Locate platelets.
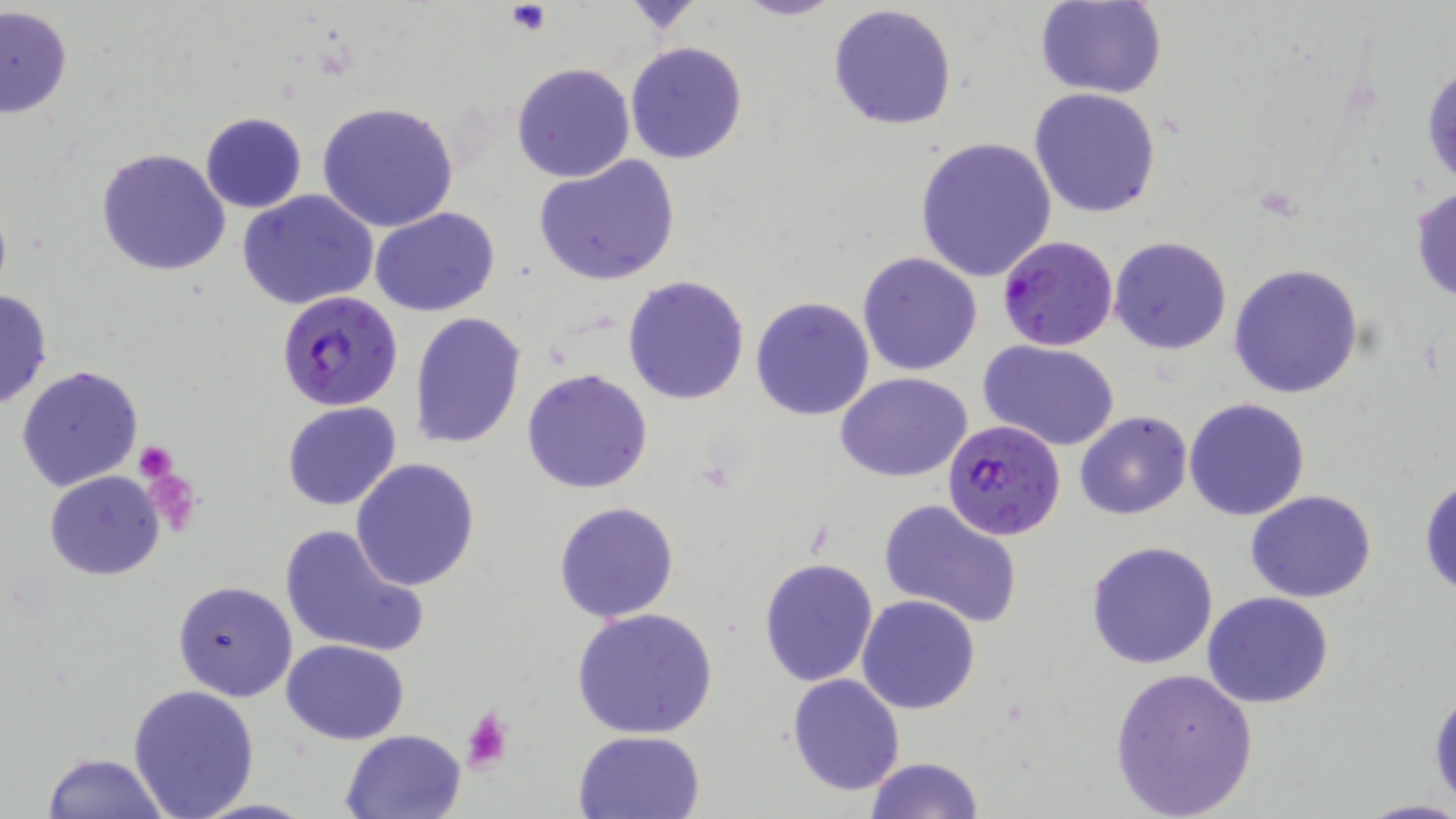

Approximate bounding boxes as (x1,y1)-(x2,y2) corner pairs in pixels.
Platelets: (506,3)-(549,33), (134,440)-(177,483), (458,705)-(512,773).

Uninfected red blood cell locations: (731,0)-(846,22), (1036,0)-(1167,99), (828,3)-(959,131), (0,6)-(73,120), (624,41)-(748,164), (1422,59)-(1456,194), (511,62)-(637,184), (1028,86)-(1162,218), (316,100)-(459,232), (199,112)-(307,213), (913,136)-(1058,283), (95,147)-(232,276), (534,154)-(680,286), (1409,184)-(1456,305), (238,191)-(379,312), (370,206)-(499,316), (1110,236)-(1233,354), (858,252)-(982,375), (1230,263)-(1364,399), (622,275)-(750,406), (0,289)-(52,410), (750,296)-(875,421), (409,312)-(526,448), (977,339)-(1122,453), (16,365)-(144,493), (521,368)-(653,495), (835,372)-(974,481), (1184,398)-(1311,520), (281,400)-(401,511), (1075,410)-(1192,520), (351,457)-(479,590), (45,470)-(165,581), (1419,473)-(1455,599), (1246,490)-(1378,603), (876,497)-(1025,629), (552,501)-(681,623), (278,523)-(430,658), (1085,540)-(1218,669), (758,556)-(880,687), (172,579)-(297,703), (1202,592)-(1335,709), (857,594)-(981,714), (570,606)-(718,741), (282,639)-(410,744), (1109,665)-(1260,818), (787,673)-(905,794), (1429,681)-(1456,814), (126,683)-(260,819), (340,727)-(468,819), (573,729)-(705,817), (42,751)-(169,819), (863,756)-(984,819), (1358,800)-(1456,819). Plasmodium falciparum-infected red blood cell locations: (997,234)-(1119,352), (276,291)-(401,411), (941,419)-(1067,540). Slide-level diagnosis: Plasmodium falciparum. Image is 1456×819 pixels. Optical microscopy. Thin blood smear. One field of a larger specimen. May-Grünwald-Giemsa stain. Captured at 1000x magnification.